Assess this cell for malaria.
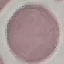
It is uninfected.

capture = smartphone camera at the microscope eyepiece
preparation = thin smear
stain = Giemsa
image type = automatically extracted cell patch, resized to 64 × 64 pixels